Give the position of every Plasmodium parasite, noting whether each is a trophozoite, schizont, or gametocyte.
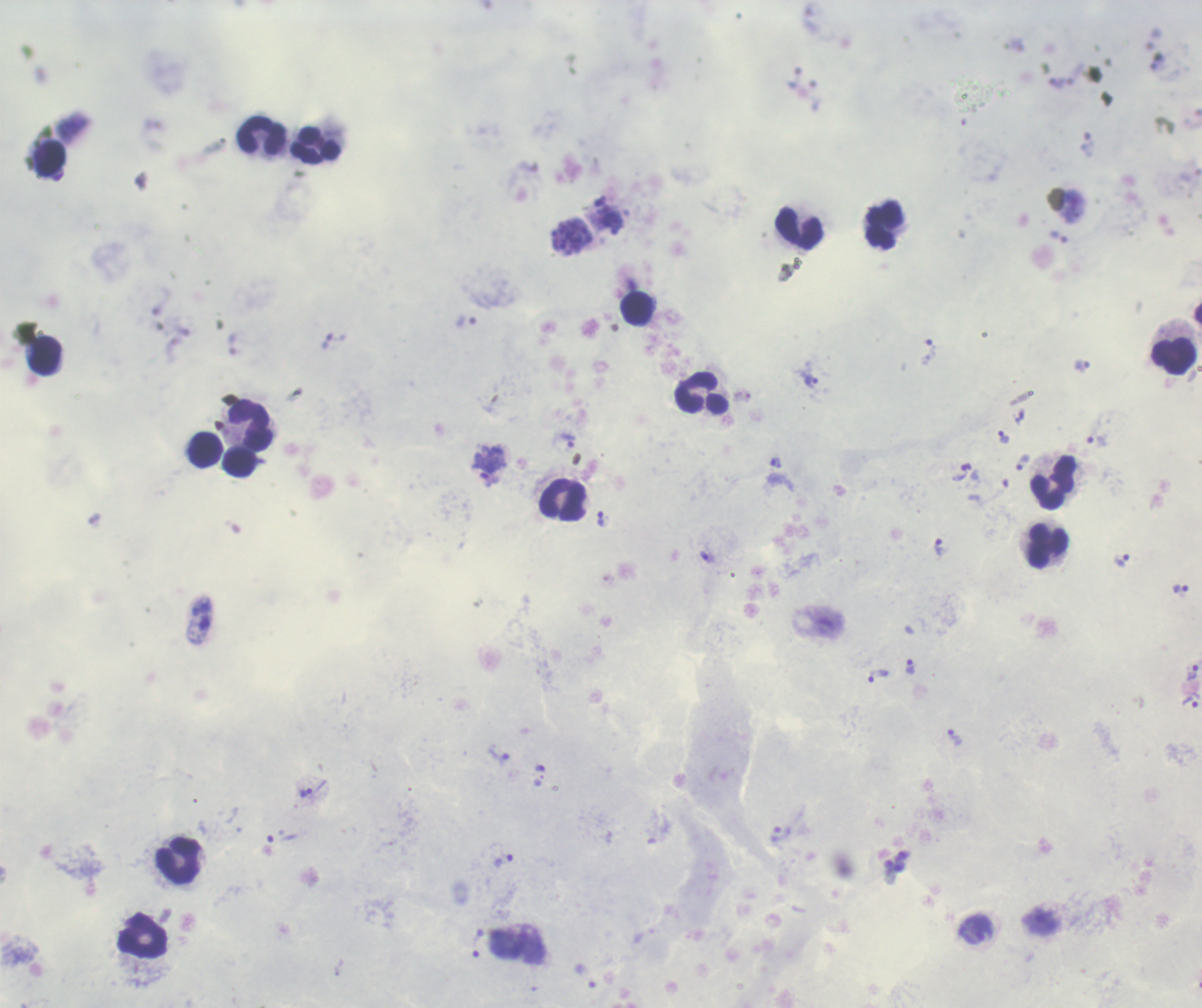

Approximate object centers, in pixels from the top-left corner.
Trophozoites: (x=1058, y=237), (x=332, y=340), (x=928, y=351), (x=1082, y=366), (x=811, y=383), (x=1003, y=436), (x=569, y=442), (x=1097, y=442), (x=776, y=462), (x=1022, y=463), (x=489, y=464), (x=960, y=473), (x=599, y=517), (x=939, y=545), (x=707, y=557), (x=1123, y=560), (x=1180, y=588), (x=909, y=666), (x=1193, y=673), (x=878, y=676), (x=1190, y=702), (x=953, y=737), (x=499, y=756), (x=306, y=793), (x=504, y=861), (x=975, y=931), (x=478, y=944).
Schizonts: (x=571, y=236).
No gametocyte forms observed.

Approximate object centers, in pixels from the top-left corner. Leukocyte locations: (x=262, y=135), (x=316, y=145), (x=51, y=159), (x=885, y=225), (x=799, y=228), (x=637, y=309), (x=45, y=355), (x=1174, y=356), (x=702, y=394), (x=250, y=425), (x=206, y=449), (x=240, y=462), (x=1054, y=483), (x=563, y=500), (x=1047, y=546), (x=178, y=861), (x=143, y=936). Thick blood smear. Image is 1202×1008 pixels. Background quality: satisfactory. Single field of view. Coloration quality: good. 100x magnification. Romanowsky-stained preparation. Previously used in a real diagnosis.